Assess this cell for malaria.
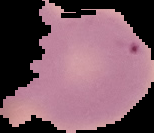

It is uninfected.

{
  "image_size": "154×133 pixels",
  "preparation": "thin blood smear",
  "image_type": "cell region segmented out of the field of view; surrounding area masked to black"
}